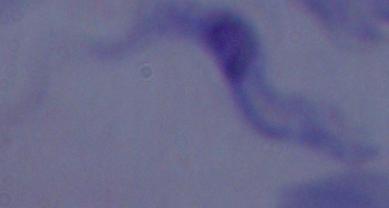

{
  "identification": "trypanosome",
  "magnification": "1000x",
  "modality": "photomicrograph"
}